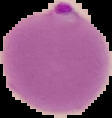

From a thin blood smear. Segmented cell region on a black background. Result: Plasmodium parasites detected. Image is 112×118 pixels.